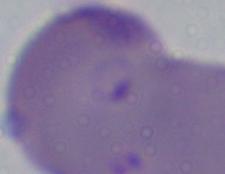

A Babesia parasite is seen. 1000x magnification. Photomicrograph.